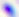

magnification: 400x
identification: Toxoplasma gondii
modality: micrograph